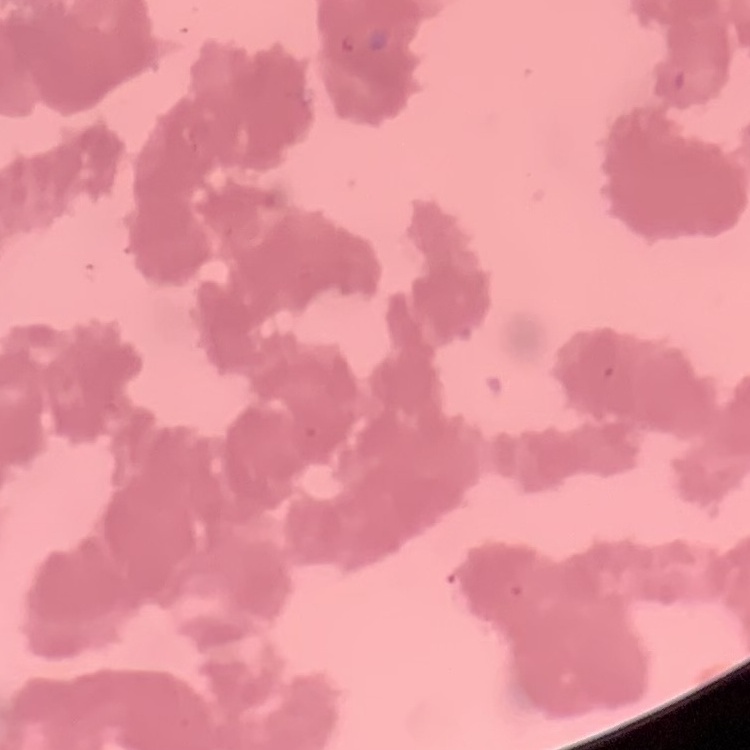
Summary:
  - Erythrocyte morphology: rouleaux formation
  - Preparation: thin peripheral smear
  - Image type: square crop of a larger photomicrograph
  - Stain: Field's or Giemsa